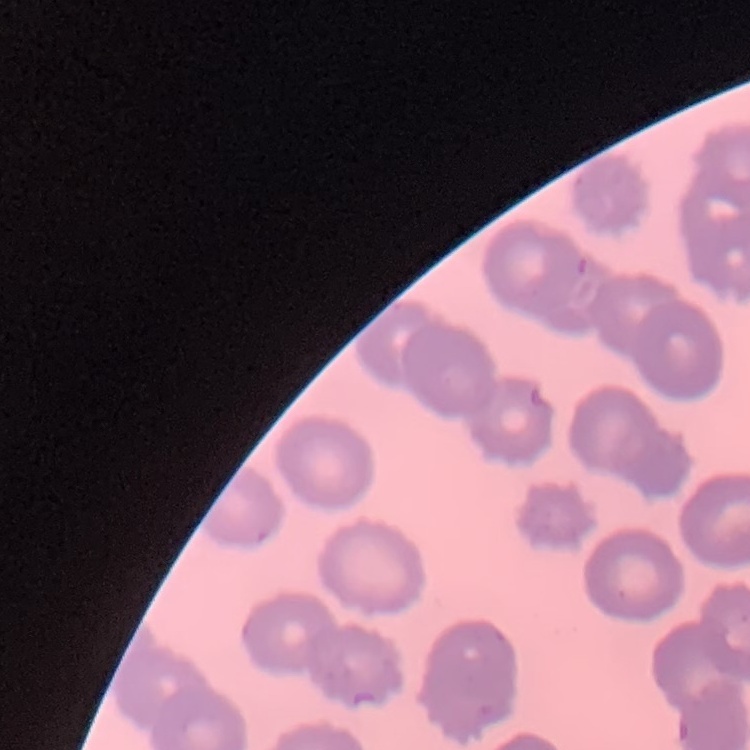
The erythrocytes exhibit no rouleaux formation. Stained with either Field's or Giemsa. Square crop of a larger photomicrograph. Thin blood film.